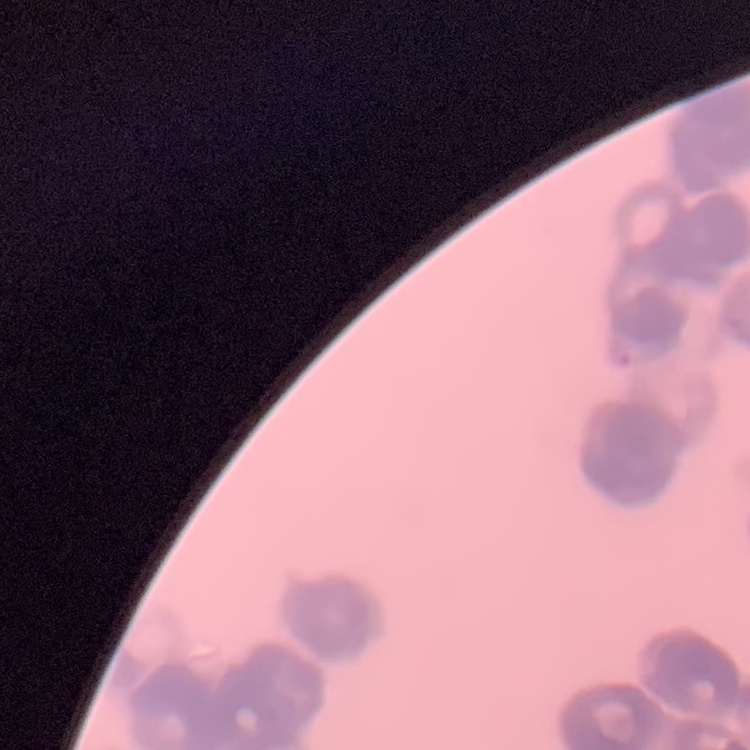

Summary:
  - Red blood cell morphology: rouleaux formation
  - Stain: Field's or Giemsa
  - Preparation: thin peripheral smear
  - Image type: one tile cut from a larger photomicrograph